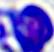

identification = leukocyte
magnification = 400x
modality = micrograph